Locate and identify every blood parasite.
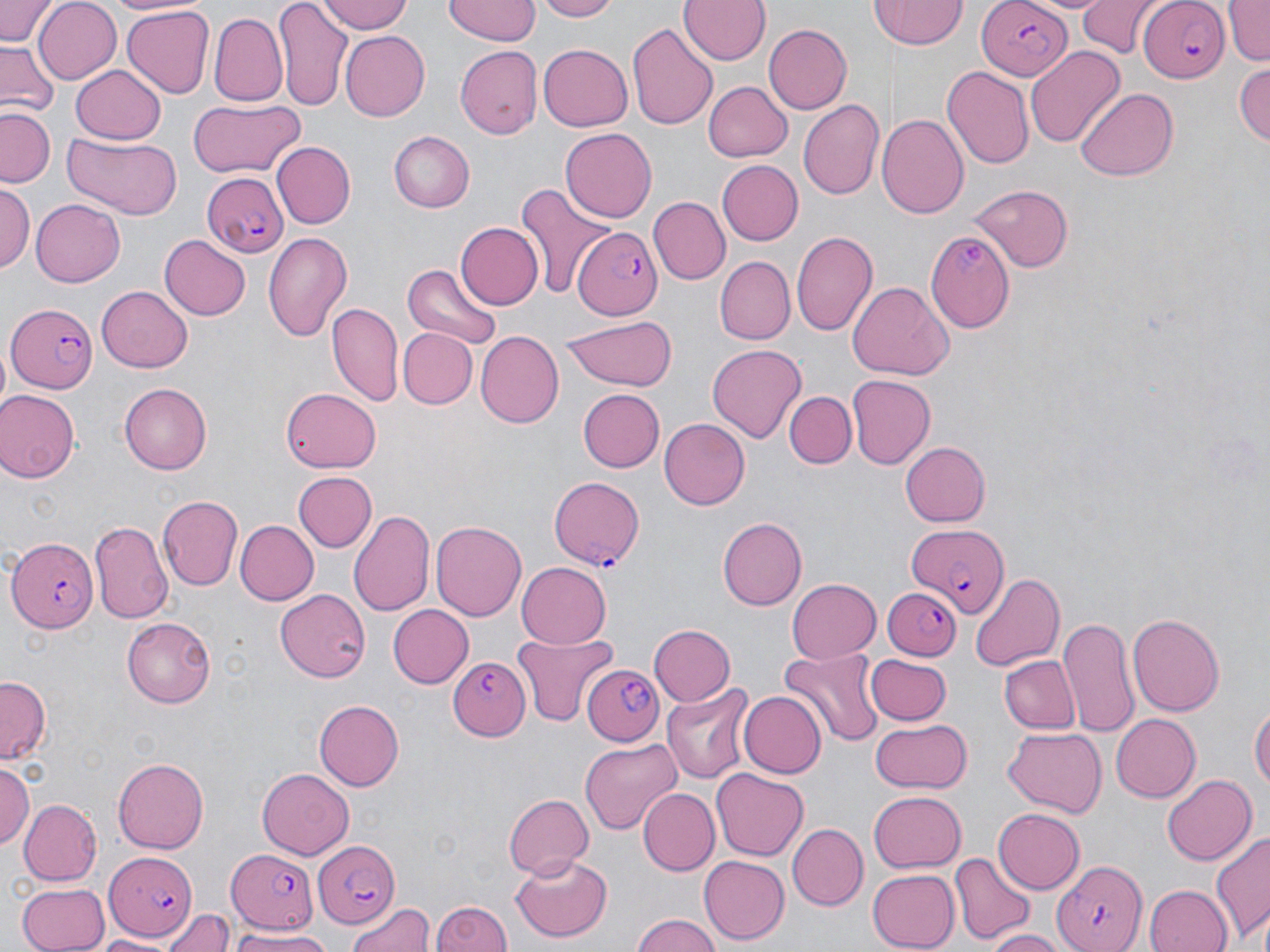
Approximate bounding boxes as [x1, y1, x2, y2] in pixels.
Plasmodium falciparum-infected red blood cells: [1136, 0, 1229, 81], [975, 1, 1072, 79], [198, 172, 290, 258], [572, 229, 661, 318], [926, 229, 1015, 331], [7, 305, 99, 393], [549, 474, 644, 566], [904, 521, 1011, 616], [7, 537, 97, 634], [883, 586, 962, 661], [447, 658, 529, 740], [583, 663, 664, 744], [312, 841, 400, 927], [221, 845, 323, 936], [104, 851, 196, 940], [1053, 860, 1147, 952].
No Plasmodium ovale, Plasmodium malariae, Plasmodium vivax, Babesia divergens, or Trypanosoma brucei observed.

Uninfected red blood cell locations: [0, 0, 59, 47], [104, 0, 202, 17], [316, 0, 414, 34], [445, 0, 543, 45], [537, 0, 620, 22], [679, 0, 773, 67], [1075, 0, 1163, 57], [1225, 0, 1270, 64], [31, 1, 121, 85], [272, 1, 353, 110], [871, 2, 969, 50], [121, 6, 212, 97], [208, 14, 287, 107], [628, 21, 719, 132], [761, 23, 851, 115], [340, 30, 431, 120], [0, 42, 63, 117], [538, 42, 633, 131], [455, 45, 543, 136], [1025, 46, 1123, 146], [1234, 61, 1269, 148], [69, 65, 166, 144], [942, 66, 1035, 169], [700, 80, 792, 163], [1077, 87, 1179, 181], [185, 100, 305, 178], [800, 100, 885, 201], [1, 108, 57, 187], [878, 112, 971, 218], [561, 127, 656, 219], [389, 130, 475, 212], [61, 134, 184, 218], [270, 142, 354, 230], [716, 161, 804, 246], [970, 182, 1074, 270], [515, 183, 613, 297], [0, 185, 34, 275], [31, 198, 127, 287], [647, 198, 730, 285], [455, 221, 543, 311], [790, 230, 877, 337], [262, 231, 354, 343], [161, 233, 249, 320], [714, 256, 794, 345], [403, 263, 503, 350], [848, 281, 952, 382], [95, 285, 192, 373], [328, 302, 403, 408], [563, 312, 678, 391], [399, 328, 476, 409], [474, 331, 562, 427], [707, 344, 807, 444], [847, 376, 935, 469], [119, 383, 211, 473], [282, 385, 382, 472], [577, 389, 665, 473], [0, 390, 81, 484], [784, 391, 856, 468], [659, 419, 749, 510], [899, 441, 991, 526], [295, 473, 376, 551], [156, 493, 243, 588], [348, 508, 435, 621], [720, 517, 809, 610], [234, 519, 319, 606], [429, 519, 528, 622], [91, 522, 172, 620], [516, 561, 611, 647], [968, 573, 1066, 672], [786, 578, 881, 662], [276, 589, 370, 682], [388, 605, 473, 688], [1126, 613, 1225, 717], [122, 617, 214, 707], [1061, 617, 1141, 740], [647, 623, 736, 707], [511, 633, 617, 727], [780, 646, 885, 745], [999, 655, 1079, 735], [869, 656, 951, 724], [0, 678, 50, 761], [661, 683, 755, 785], [739, 692, 826, 777], [313, 699, 402, 791], [1250, 699, 1269, 795], [1108, 715, 1199, 802], [868, 718, 972, 794], [1002, 728, 1105, 817], [578, 737, 682, 835], [112, 756, 210, 853], [1, 761, 34, 853], [712, 767, 809, 860], [257, 768, 355, 860], [1160, 773, 1258, 868], [638, 789, 717, 875], [868, 791, 966, 872], [502, 794, 593, 879], [20, 799, 103, 884], [992, 809, 1083, 895], [789, 823, 866, 909], [1212, 831, 1270, 947], [950, 853, 1034, 944], [511, 856, 613, 942], [698, 856, 788, 944], [867, 867, 961, 949], [15, 881, 108, 951], [1144, 883, 1233, 952], [432, 897, 512, 952], [345, 899, 434, 950], [160, 906, 237, 952], [629, 914, 724, 952], [228, 927, 338, 951], [983, 928, 1067, 952], [91, 932, 180, 950]. Slide-level diagnosis: Plasmodium falciparum. Image is 1270×952 pixels. Light microscopy. Single field of view. May-Grünwald-Giemsa stain. 1000x magnification. Thin blood smear.